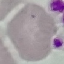
Malaria status: uninfected. Giemsa stain. Photographed with a smartphone camera at the microscope eyepiece. Cell patch, automatically extracted from a larger field of view and resized to 64 × 64 pixels. Thin blood smear.